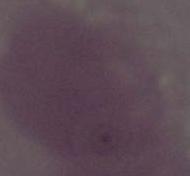

1000x magnification. An erythrocyte is shown. Photomicrograph.